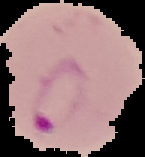

Image is 145×157 pixels. From a thin blood film. Segmented cell region on a black background. Malaria status: parasitized.